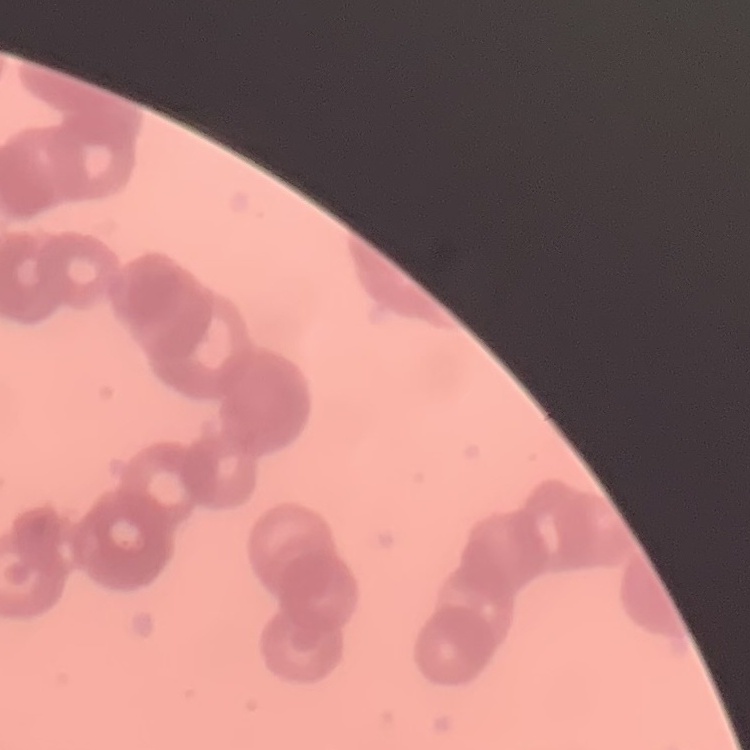
Summary:
  - Red blood cell morphology: rouleaux formation
  - Stain: Field's or Giemsa
  - Preparation: thin blood film
  - Image type: square crop of a larger photomicrograph